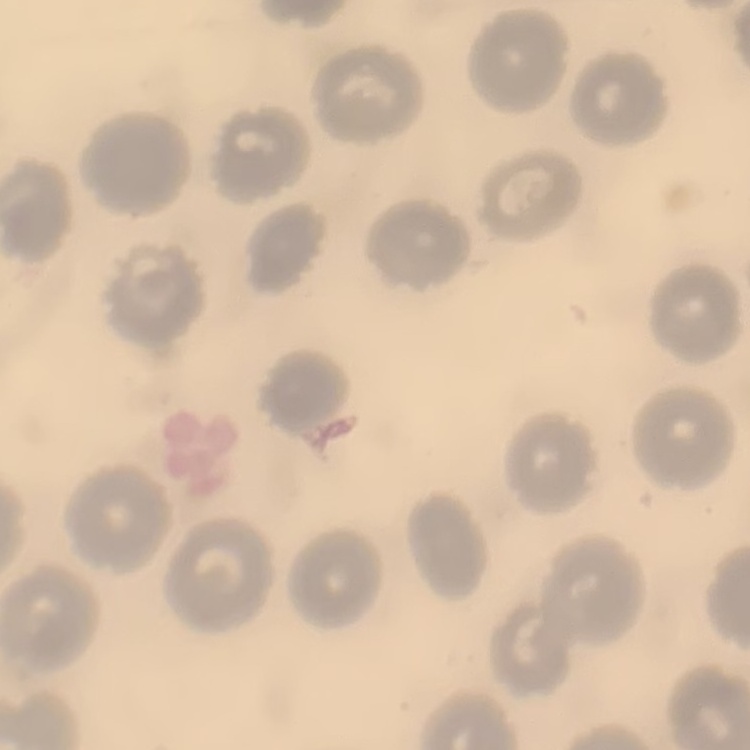
Summary:
  - Erythrocyte morphology: no rouleaux formation
  - Preparation: thin blood film
  - Image type: one tile cut from a larger photomicrograph
  - Stain: Field's or Giemsa